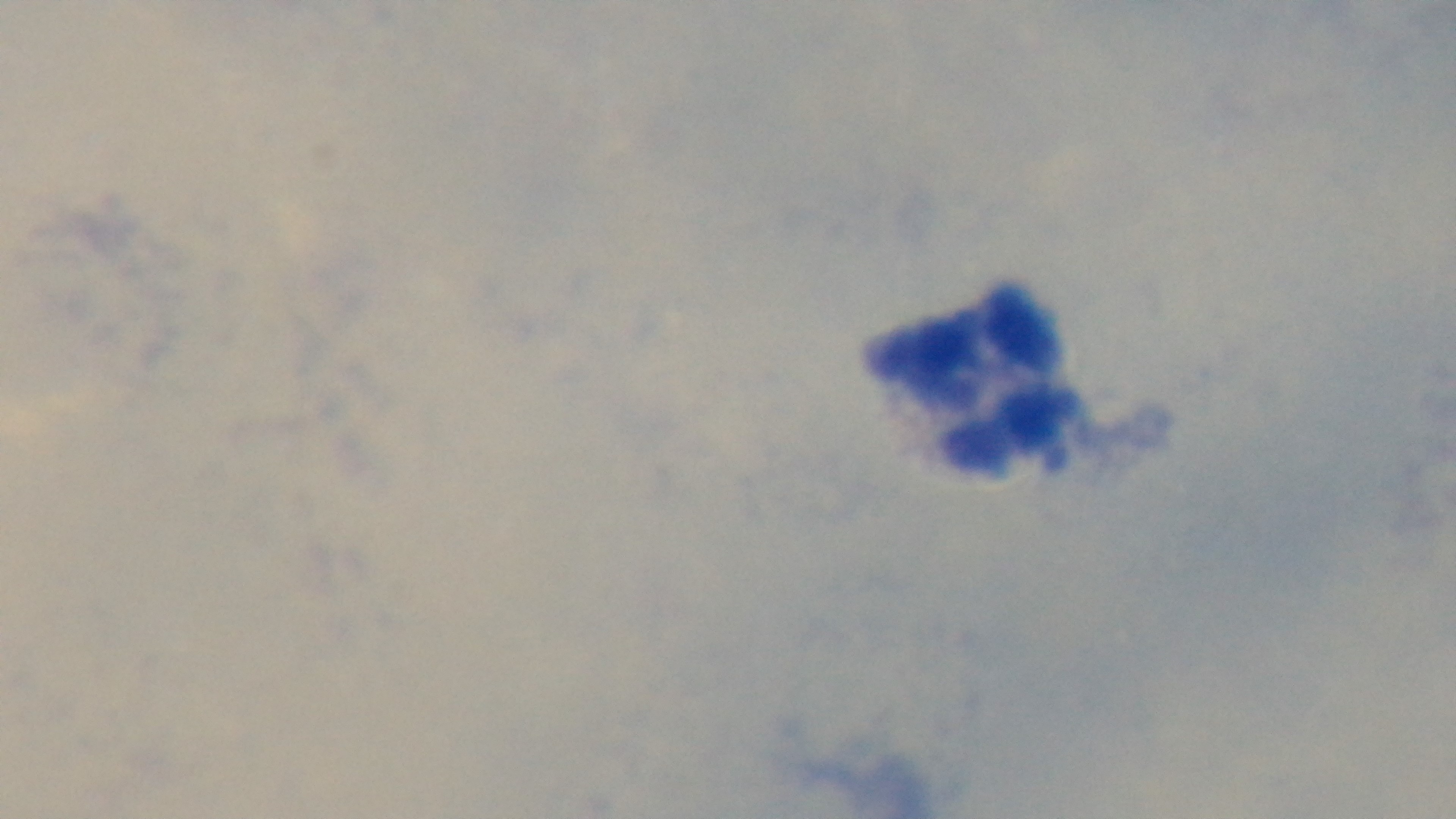 Single field of view. Malaria status: uninfected. Mounted 4K digital camera. Photomicrograph. Giemsa stain. 100x oil-immersion objective. Preparation: thick.